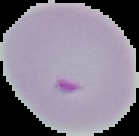
Summary:
  - Image size: 139×136 pixels
  - Result: malaria parasites detected
  - Image type: segmented cell region with the area outside set to black
  - Preparation: thin blood smear